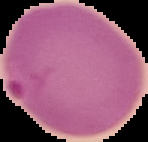

image type = segmented cell region with the area outside set to black
preparation = thin blood film
result = malaria parasites detected
image size = 148×142 pixels